Locate and identify every blood parasite.
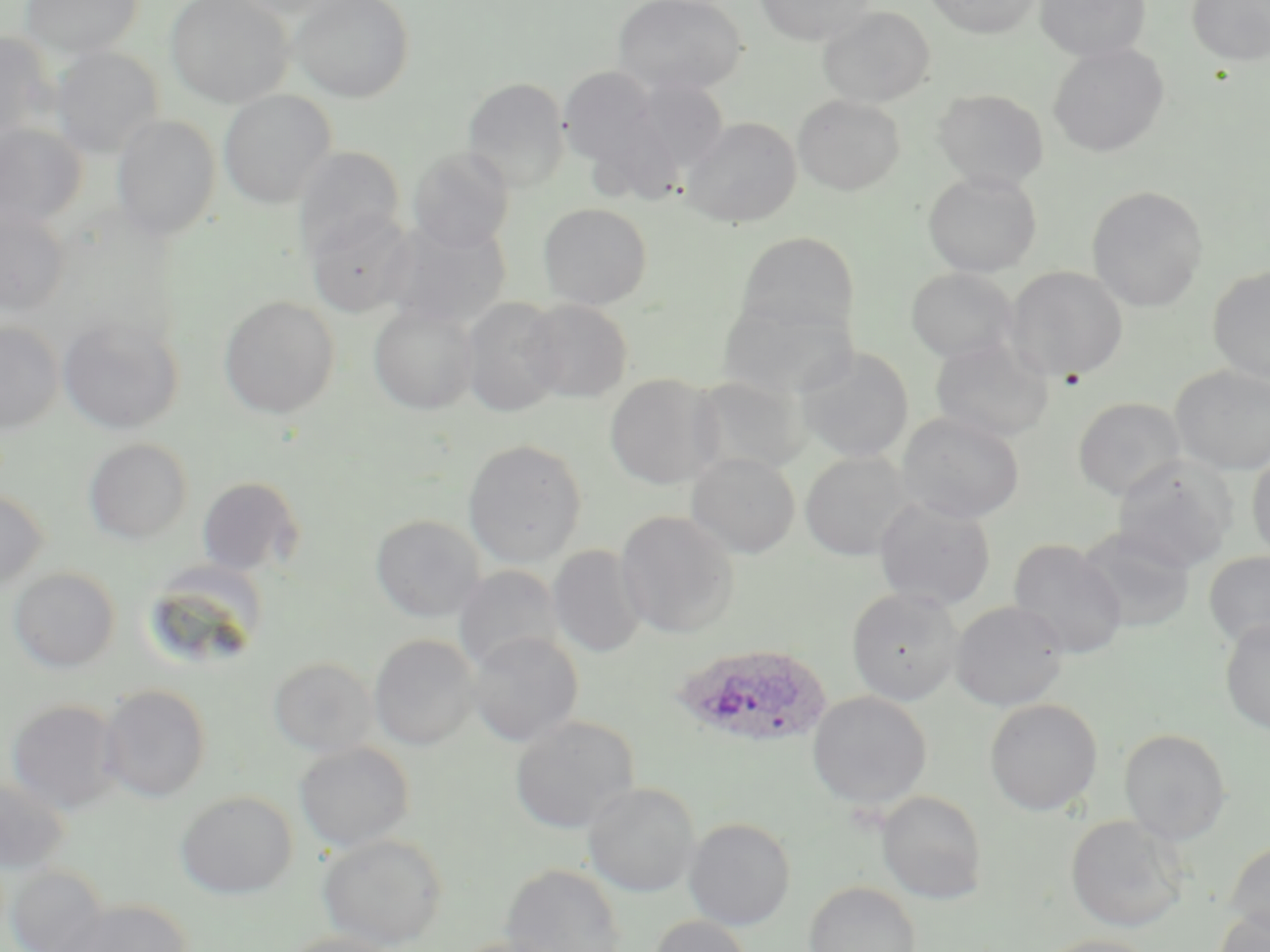
Approximate bounding boxes as named x1/y1/x2/y2 corners in pixels.
Plasmodium ovale-infected red blood cells: (x1=671, y1=642, x2=834, y2=749).
No Plasmodium falciparum, Plasmodium malariae, Plasmodium vivax, Babesia divergens, or Trypanosoma brucei observed.

slide-level diagnosis = Plasmodium ovale
modality = light microscopy
image size = 1270×952 pixels
field of view = one of a larger specimen
preparation = thin blood smear
stain = May-Grünwald-Giemsa
uninfected red blood cell locations = approximate bounding boxes as named x1/y1/x2/y2 corners in pixels: (x1=21, y1=0, x2=143, y2=59), (x1=165, y1=0, x2=294, y2=108), (x1=225, y1=0, x2=355, y2=19), (x1=289, y1=0, x2=415, y2=103), (x1=612, y1=0, x2=748, y2=96), (x1=755, y1=0, x2=876, y2=45), (x1=925, y1=0, x2=1042, y2=38), (x1=1034, y1=0, x2=1151, y2=62), (x1=1187, y1=0, x2=1270, y2=66), (x1=817, y1=6, x2=935, y2=107), (x1=0, y1=32, x2=55, y2=141), (x1=1048, y1=42, x2=1169, y2=157), (x1=51, y1=46, x2=163, y2=159), (x1=558, y1=66, x2=662, y2=170), (x1=631, y1=76, x2=730, y2=175), (x1=462, y1=77, x2=570, y2=192), (x1=934, y1=88, x2=1049, y2=192), (x1=219, y1=90, x2=336, y2=209), (x1=793, y1=95, x2=905, y2=195), (x1=111, y1=114, x2=221, y2=241), (x1=682, y1=117, x2=802, y2=228), (x1=0, y1=123, x2=86, y2=231), (x1=294, y1=147, x2=405, y2=255), (x1=408, y1=147, x2=515, y2=251), (x1=923, y1=170, x2=1042, y2=277), (x1=1086, y1=186, x2=1208, y2=312), (x1=538, y1=203, x2=653, y2=310), (x1=0, y1=209, x2=70, y2=316), (x1=306, y1=210, x2=416, y2=318), (x1=382, y1=218, x2=511, y2=328), (x1=735, y1=230, x2=860, y2=340), (x1=1005, y1=266, x2=1128, y2=381), (x1=1207, y1=266, x2=1270, y2=385), (x1=906, y1=267, x2=1018, y2=364), (x1=219, y1=296, x2=340, y2=418), (x1=461, y1=297, x2=565, y2=416), (x1=716, y1=297, x2=856, y2=401), (x1=522, y1=300, x2=633, y2=402), (x1=369, y1=304, x2=478, y2=415), (x1=58, y1=316, x2=184, y2=434), (x1=0, y1=320, x2=64, y2=434), (x1=930, y1=337, x2=1054, y2=443), (x1=795, y1=345, x2=915, y2=463), (x1=1170, y1=366, x2=1270, y2=474), (x1=604, y1=373, x2=723, y2=489), (x1=688, y1=375, x2=811, y2=477), (x1=1072, y1=397, x2=1186, y2=501), (x1=896, y1=412, x2=1024, y2=523), (x1=84, y1=438, x2=193, y2=545), (x1=463, y1=440, x2=587, y2=567), (x1=1247, y1=449, x2=1270, y2=561), (x1=800, y1=451, x2=916, y2=560), (x1=686, y1=452, x2=800, y2=558), (x1=1112, y1=457, x2=1236, y2=573), (x1=196, y1=475, x2=305, y2=578), (x1=0, y1=487, x2=48, y2=593), (x1=874, y1=497, x2=996, y2=611), (x1=616, y1=510, x2=740, y2=639), (x1=371, y1=514, x2=485, y2=623), (x1=1075, y1=526, x2=1196, y2=632), (x1=1007, y1=538, x2=1127, y2=660), (x1=548, y1=545, x2=647, y2=658), (x1=1203, y1=551, x2=1270, y2=649), (x1=139, y1=563, x2=268, y2=674), (x1=453, y1=565, x2=565, y2=673), (x1=9, y1=568, x2=120, y2=674), (x1=846, y1=586, x2=964, y2=706), (x1=951, y1=601, x2=1069, y2=711), (x1=1220, y1=618, x2=1270, y2=733), (x1=466, y1=631, x2=584, y2=747), (x1=369, y1=634, x2=479, y2=750), (x1=268, y1=657, x2=379, y2=758), (x1=98, y1=684, x2=212, y2=803), (x1=807, y1=691, x2=932, y2=811), (x1=6, y1=698, x2=122, y2=814), (x1=984, y1=698, x2=1103, y2=816), (x1=509, y1=715, x2=640, y2=835), (x1=1119, y1=728, x2=1232, y2=845), (x1=295, y1=742, x2=415, y2=852), (x1=0, y1=777, x2=71, y2=873), (x1=583, y1=782, x2=701, y2=897), (x1=176, y1=791, x2=297, y2=898), (x1=875, y1=791, x2=988, y2=905), (x1=1065, y1=815, x2=1189, y2=932), (x1=684, y1=818, x2=796, y2=930), (x1=317, y1=833, x2=449, y2=950), (x1=1224, y1=840, x2=1270, y2=938), (x1=501, y1=863, x2=626, y2=952), (x1=6, y1=866, x2=110, y2=952), (x1=804, y1=880, x2=921, y2=952), (x1=60, y1=898, x2=195, y2=952), (x1=1211, y1=907, x2=1270, y2=952), (x1=648, y1=915, x2=754, y2=952), (x1=279, y1=931, x2=402, y2=952), (x1=1039, y1=934, x2=1156, y2=952), (x1=449, y1=935, x2=570, y2=952)
magnification = 1000x